Identify the parasite.
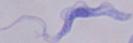

This is a trypanosome.

Summary:
  - Magnification: 1000x
  - Modality: photomicrograph